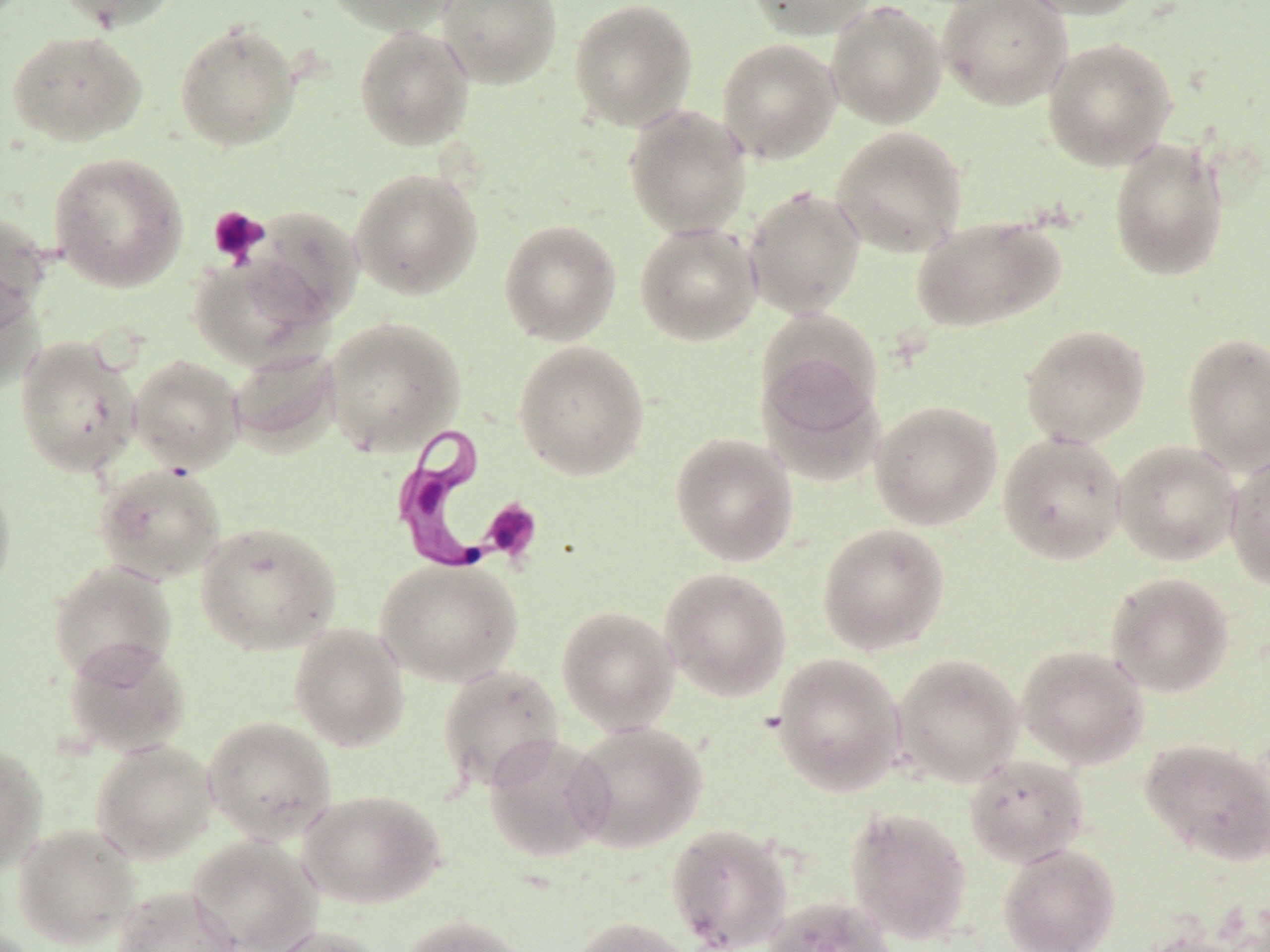
Summary:
  - Coordinate format: approximate bounding boxes as (x1, y1, x2, y2) in pixels
  - Uninfected red blood cell locations: (54, 0, 181, 32), (324, 0, 462, 35), (437, 0, 562, 89), (568, 0, 698, 131), (744, 0, 876, 41), (938, 0, 1072, 110), (1014, 0, 1150, 20), (826, 2, 947, 128), (174, 21, 301, 151), (354, 24, 474, 151), (7, 30, 147, 146), (1042, 37, 1177, 170), (717, 38, 842, 164), (623, 105, 752, 238), (830, 126, 968, 258), (1108, 137, 1230, 282), (48, 152, 188, 292), (349, 168, 483, 300), (743, 186, 866, 319), (246, 207, 364, 328), (0, 211, 51, 331), (910, 216, 1066, 333), (499, 219, 621, 345), (635, 222, 761, 346), (188, 255, 327, 370), (0, 277, 44, 396), (323, 316, 465, 455), (1020, 324, 1151, 447), (1181, 332, 1270, 474), (15, 336, 141, 477), (513, 340, 650, 480), (227, 347, 342, 455), (114, 351, 233, 585), (129, 355, 244, 474), (869, 400, 1003, 531), (669, 432, 799, 566), (997, 432, 1127, 565), (1113, 440, 1241, 566), (1225, 452, 1270, 591), (94, 463, 226, 584), (0, 473, 16, 602), (195, 521, 341, 655), (817, 522, 950, 655), (376, 557, 523, 686), (47, 561, 177, 684), (659, 566, 792, 701), (1105, 572, 1235, 698), (556, 605, 679, 734), (288, 622, 410, 752), (63, 638, 191, 757), (1016, 644, 1150, 769), (770, 652, 906, 796), (892, 653, 1023, 788), (437, 664, 565, 793), (202, 716, 337, 844), (567, 721, 708, 854), (483, 732, 612, 864), (1140, 737, 1270, 866), (91, 739, 217, 863), (0, 743, 47, 874), (963, 753, 1090, 867), (298, 789, 446, 909), (845, 807, 973, 945), (13, 823, 141, 948), (665, 823, 793, 951), (187, 836, 322, 952), (997, 843, 1121, 952), (113, 885, 242, 952), (761, 896, 898, 952), (399, 914, 534, 952), (570, 916, 697, 952), (265, 925, 388, 952), (1136, 932, 1255, 952)
  - Trypanosoma brucei locations: (391, 421, 539, 575)
  - Platelet locations: (207, 205, 270, 267), (479, 498, 543, 564)
  - Slide-level diagnosis: Trypanosoma brucei
  - Field of view: single
  - Modality: light microscopy
  - Preparation: thin blood film
  - Stain: May-Grünwald-Giemsa
  - Magnification: 1000x
  - Image size: 1270×952 pixels